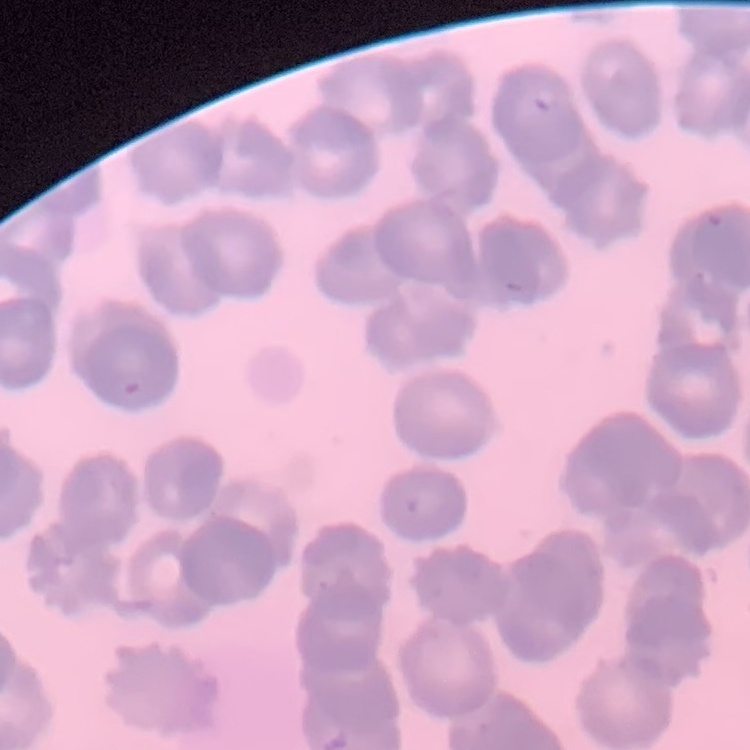
{
  "erythrocyte_morphology": "rouleaux formation",
  "image_type": "one tile cut from a larger photomicrograph",
  "preparation": "thin peripheral smear",
  "stain": "Field's or Giemsa"
}